Report the malaria status of this cell.
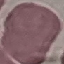
Uninfected.

Summary:
  - Preparation: thin blood film
  - Capture: smartphone through the microscope eyepiece
  - Stain: Giemsa
  - Image type: automatically extracted cell patch, resized to 64 × 64 pixels